Assess the morphology of the erythrocytes.
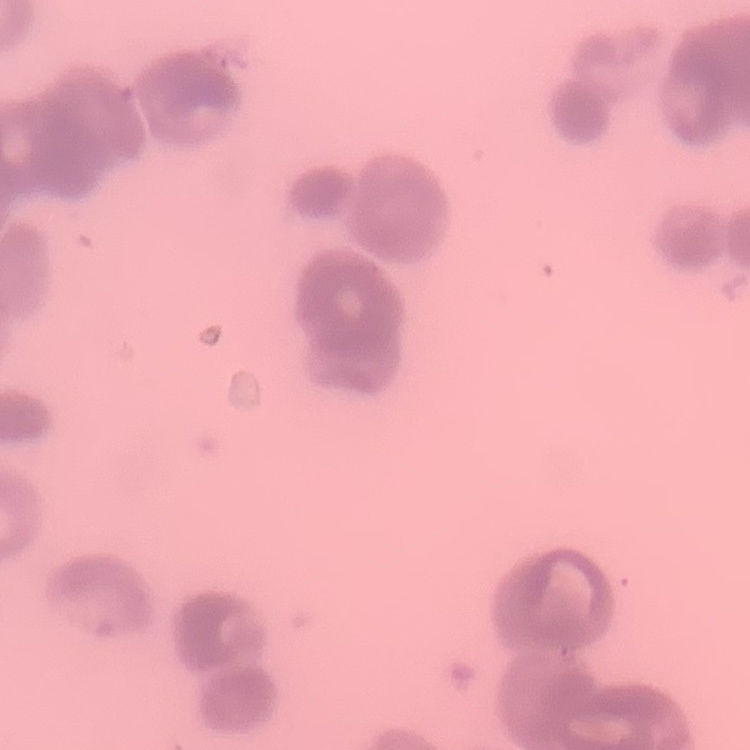
They show rouleaux formation.

Summary:
  - Stain: Field's or Giemsa
  - Image type: one tile cut from a larger photomicrograph
  - Preparation: thin blood smear